Name the blood parasite species.
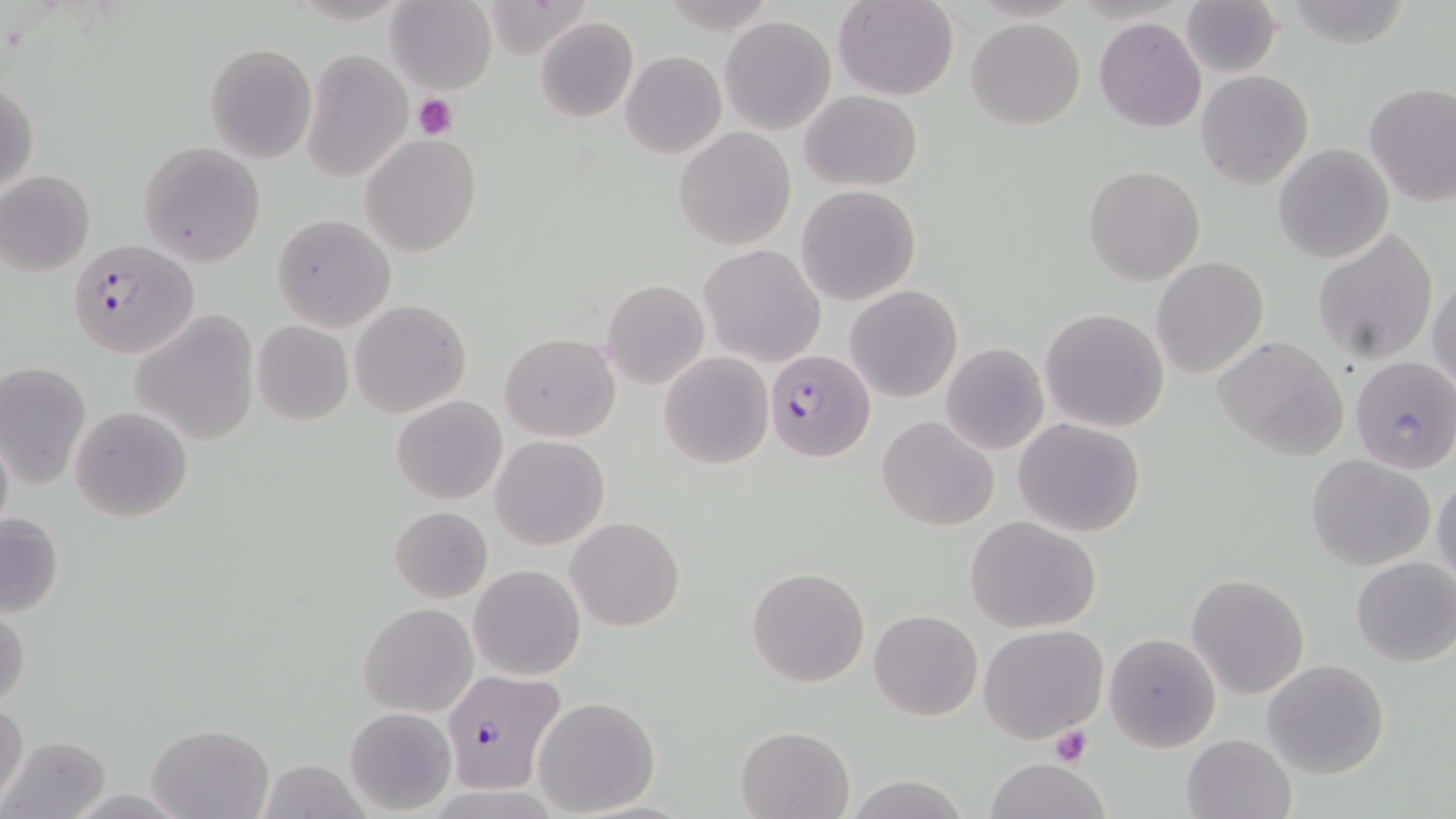
Plasmodium falciparum.

modality = light microscopy
uninfected red blood cell locations = approximate bounding boxes as named x1/y1/x2/y2 corners in pixels: (x1=387, y1=0, x2=497, y2=93), (x1=832, y1=0, x2=959, y2=100), (x1=1283, y1=0, x2=1415, y2=49), (x1=483, y1=1, x2=594, y2=62), (x1=1180, y1=2, x2=1283, y2=79), (x1=720, y1=15, x2=836, y2=135), (x1=535, y1=17, x2=639, y2=122), (x1=966, y1=17, x2=1086, y2=130), (x1=1094, y1=17, x2=1207, y2=132), (x1=204, y1=42, x2=317, y2=163), (x1=302, y1=49, x2=412, y2=183), (x1=620, y1=50, x2=727, y2=159), (x1=1195, y1=69, x2=1314, y2=190), (x1=1, y1=80, x2=37, y2=201), (x1=1362, y1=80, x2=1456, y2=206), (x1=800, y1=91, x2=923, y2=190), (x1=673, y1=126, x2=797, y2=250), (x1=360, y1=134, x2=479, y2=258), (x1=138, y1=141, x2=264, y2=266), (x1=1273, y1=144, x2=1393, y2=263), (x1=1083, y1=166, x2=1204, y2=285), (x1=1, y1=172, x2=94, y2=276), (x1=796, y1=185, x2=921, y2=306), (x1=271, y1=214, x2=396, y2=330), (x1=1312, y1=228, x2=1439, y2=364), (x1=700, y1=244, x2=824, y2=367), (x1=1150, y1=256, x2=1270, y2=378), (x1=1429, y1=275, x2=1456, y2=394), (x1=601, y1=279, x2=710, y2=389), (x1=846, y1=285, x2=963, y2=402), (x1=350, y1=300, x2=471, y2=418), (x1=1039, y1=307, x2=1170, y2=432), (x1=131, y1=312, x2=262, y2=444), (x1=251, y1=320, x2=354, y2=425), (x1=499, y1=331, x2=620, y2=443), (x1=1215, y1=334, x2=1350, y2=460), (x1=941, y1=342, x2=1049, y2=454), (x1=659, y1=351, x2=773, y2=470), (x1=1349, y1=355, x2=1456, y2=474), (x1=0, y1=360, x2=91, y2=488), (x1=392, y1=395, x2=507, y2=505), (x1=70, y1=406, x2=194, y2=522), (x1=876, y1=415, x2=999, y2=530), (x1=1013, y1=418, x2=1146, y2=537), (x1=0, y1=427, x2=13, y2=540), (x1=491, y1=435, x2=609, y2=551), (x1=1306, y1=455, x2=1437, y2=570), (x1=1432, y1=470, x2=1456, y2=591), (x1=388, y1=504, x2=492, y2=603), (x1=0, y1=509, x2=64, y2=619), (x1=965, y1=515, x2=1101, y2=635), (x1=565, y1=516, x2=685, y2=632), (x1=1350, y1=556, x2=1456, y2=667), (x1=470, y1=564, x2=585, y2=680), (x1=747, y1=565, x2=871, y2=686), (x1=1187, y1=574, x2=1308, y2=698), (x1=358, y1=602, x2=477, y2=716), (x1=0, y1=606, x2=30, y2=708), (x1=869, y1=609, x2=981, y2=720), (x1=977, y1=624, x2=1109, y2=745), (x1=1103, y1=631, x2=1221, y2=752), (x1=1263, y1=659, x2=1390, y2=779), (x1=532, y1=695, x2=660, y2=815), (x1=0, y1=699, x2=28, y2=806), (x1=344, y1=706, x2=456, y2=815), (x1=146, y1=722, x2=274, y2=817), (x1=735, y1=724, x2=855, y2=817), (x1=1180, y1=732, x2=1296, y2=819), (x1=2, y1=734, x2=110, y2=817), (x1=982, y1=758, x2=1114, y2=818), (x1=258, y1=759, x2=370, y2=818), (x1=842, y1=772, x2=969, y2=819)
stain = May-Grünwald-Giemsa
magnification = 1000x
platelet locations = approximate bounding boxes as named x1/y1/x2/y2 corners in pixels: (x1=414, y1=93, x2=458, y2=139), (x1=1048, y1=725, x2=1093, y2=767)
Plasmodium falciparum-infected red blood cell locations = approximate bounding boxes as named x1/y1/x2/y2 corners in pixels: (x1=69, y1=237, x2=197, y2=357), (x1=764, y1=348, x2=875, y2=462), (x1=442, y1=668, x2=566, y2=795)
image size = 1456×819 pixels
field of view = one of a larger specimen
preparation = thin blood film